State which parasite is depicted.
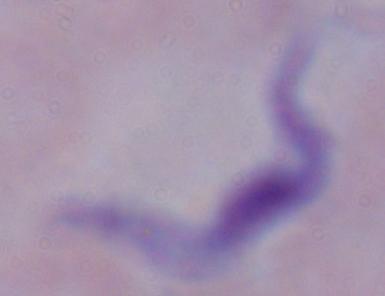

A trypanosome.

Summary:
  - Magnification: 1000x
  - Modality: micrograph